Classify this cell by malaria status.
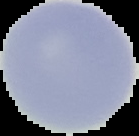
It is uninfected.

Summary:
  - Image type: cell region segmented out of the field of view; surrounding area masked to black
  - Image size: 139×136 pixels
  - Preparation: thin blood smear